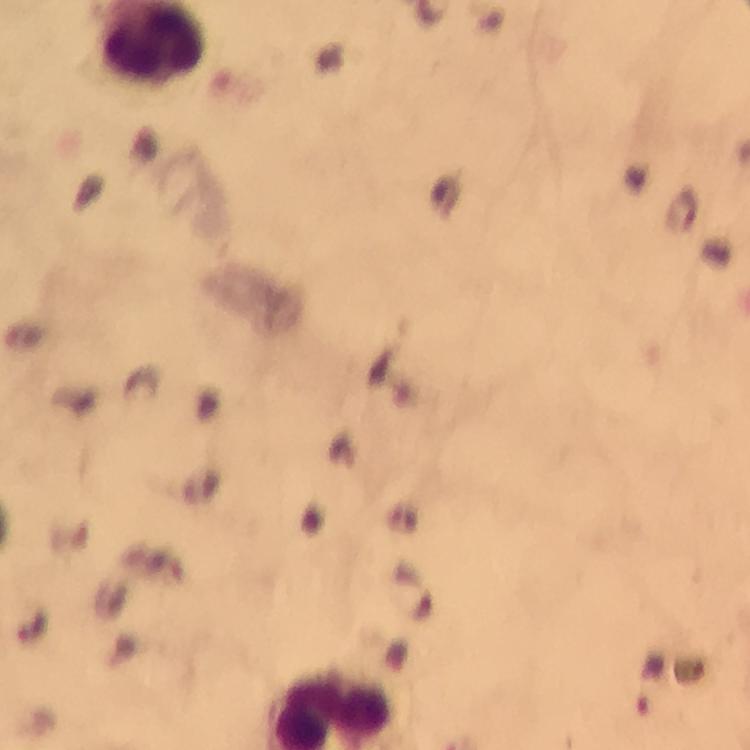

immersion oil = used
cropped from = a single field of view
malaria parasite locations = approximate centers as [x, y] in pixels: [652, 685]
preparation = thick blood film
capture = smartphone mounted on the microscope
magnification = 100x
context = from a diagnostic examination for malaria
image size = 750×750 pixels
stain = Giemsa